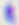

Captured at 400x magnification. Micrograph. Toxoplasma gondii is shown.